Outline each uninfected red blood cell.
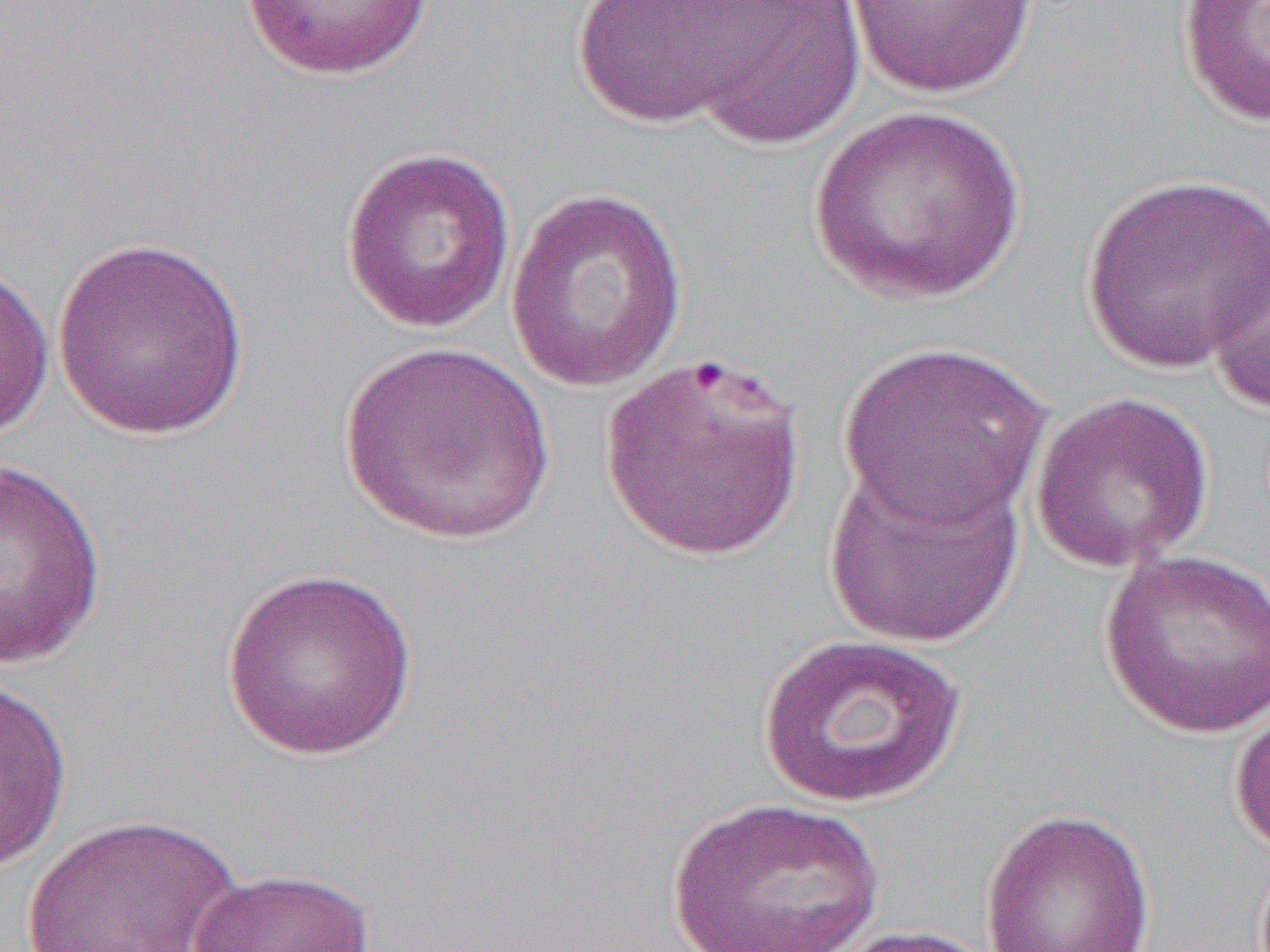

Approximate bounding boxes as (x1,y1)-(x2,y2) corner pairs in pixels.
Uninfected red blood cells: (570,0)-(783,130), (240,1)-(436,81), (677,1)-(868,149), (843,1)-(1040,99), (1176,1)-(1270,128), (808,105)-(1026,304), (340,145)-(516,335), (1080,171)-(1270,374), (504,188)-(688,392), (1205,227)-(1270,414), (51,238)-(251,442), (0,261)-(55,441), (336,340)-(558,545), (835,341)-(1053,532), (600,352)-(809,562), (1030,392)-(1214,573), (1,456)-(109,670), (823,459)-(1026,649), (1099,547)-(1270,739), (220,566)-(419,761), (756,632)-(969,809), (0,675)-(73,875), (1229,698)-(1270,859), (665,796)-(886,951), (979,807)-(1156,952), (22,813)-(245,951), (187,867)-(376,952), (824,923)-(1000,952).

{
  "slide_level_diagnosis": "Plasmodium falciparum",
  "field_of_view": "one of a larger specimen",
  "image_size": "1270×952 pixels",
  "preparation": "thin blood smear",
  "modality": "light microscopy",
  "magnification": "1000x"
}